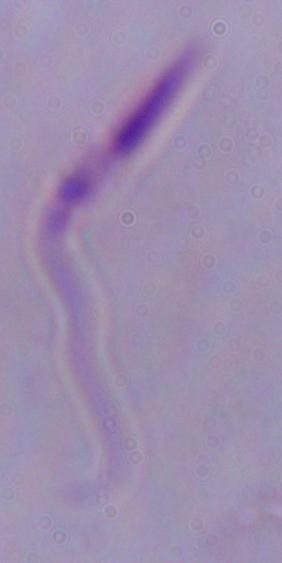
magnification: 1000x
identification: Leishmania
modality: micrograph